Name the parasite shown.
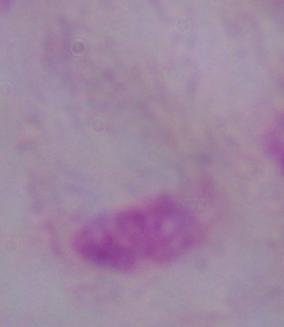

A trichomonad.

Summary:
  - Modality: photomicrograph
  - Magnification: 1000x